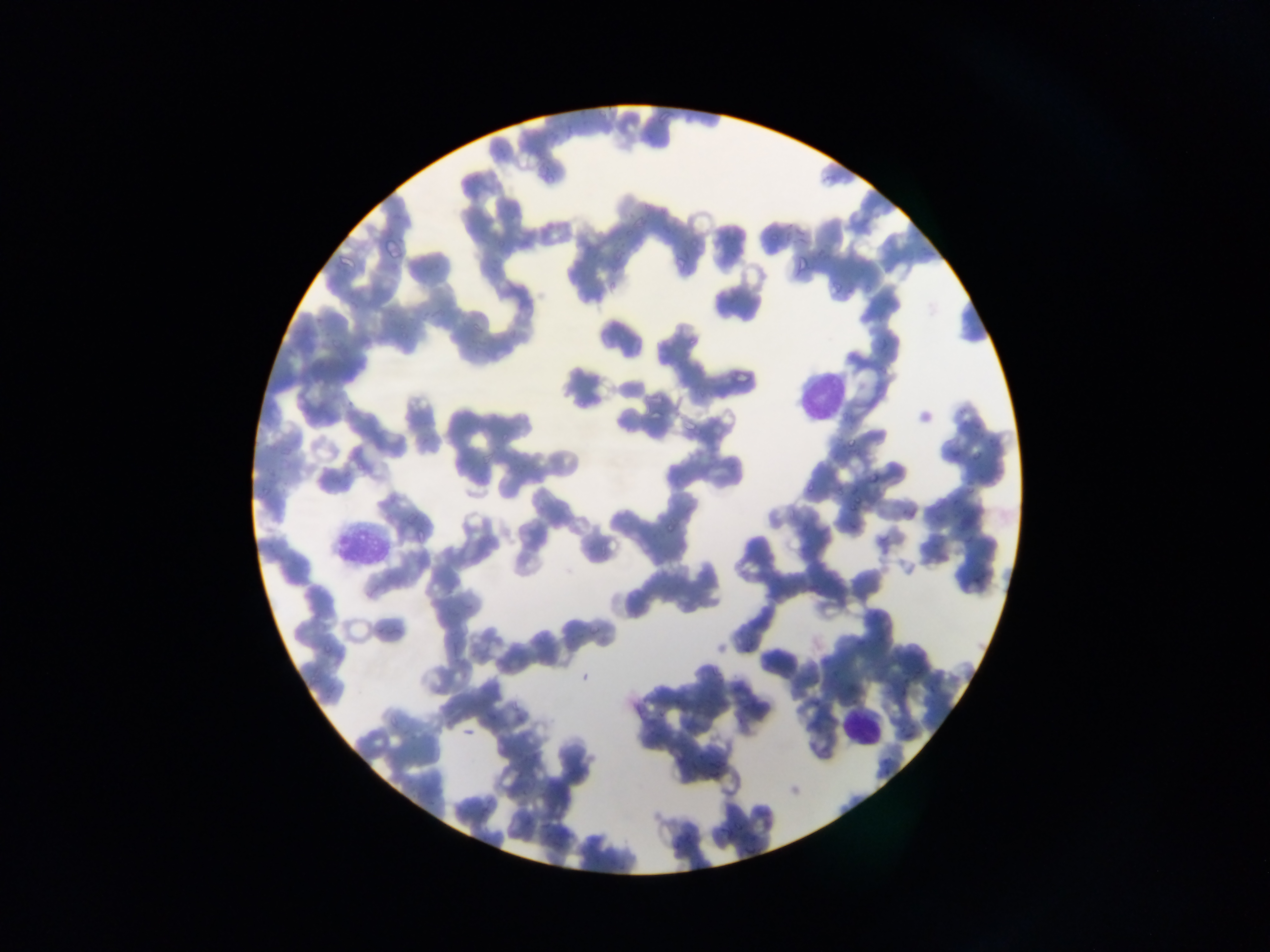
leukocyte locations = approximate bounding boxes as (left, top, right, bottom) in pixels: (787, 360, 850, 420), (324, 515, 390, 571), (833, 659, 891, 747)
country = Ghana
preparation = thin blood smear
capture = mobile-phone photograph through a microscope
image size = 1270×952 pixels
malaria parasite locations = approximate bounding boxes as (left, top, right, bottom) in pixels: (770, 236, 779, 241), (346, 394, 355, 405), (650, 407, 664, 423), (974, 424, 980, 435), (844, 437, 856, 450), (949, 444, 964, 457), (969, 453, 981, 463), (727, 459, 747, 479), (869, 469, 883, 484), (965, 483, 977, 497), (803, 484, 818, 496), (949, 495, 962, 507), (855, 496, 863, 503), (849, 505, 856, 515), (903, 505, 913, 520), (957, 513, 973, 528), (662, 521, 678, 538), (848, 521, 857, 530), (961, 537, 971, 543), (973, 576, 992, 586), (743, 640, 753, 652) | approximate (x, y) pixel centers of objects too small to bound: (526, 791), (486, 811)
field of view = single